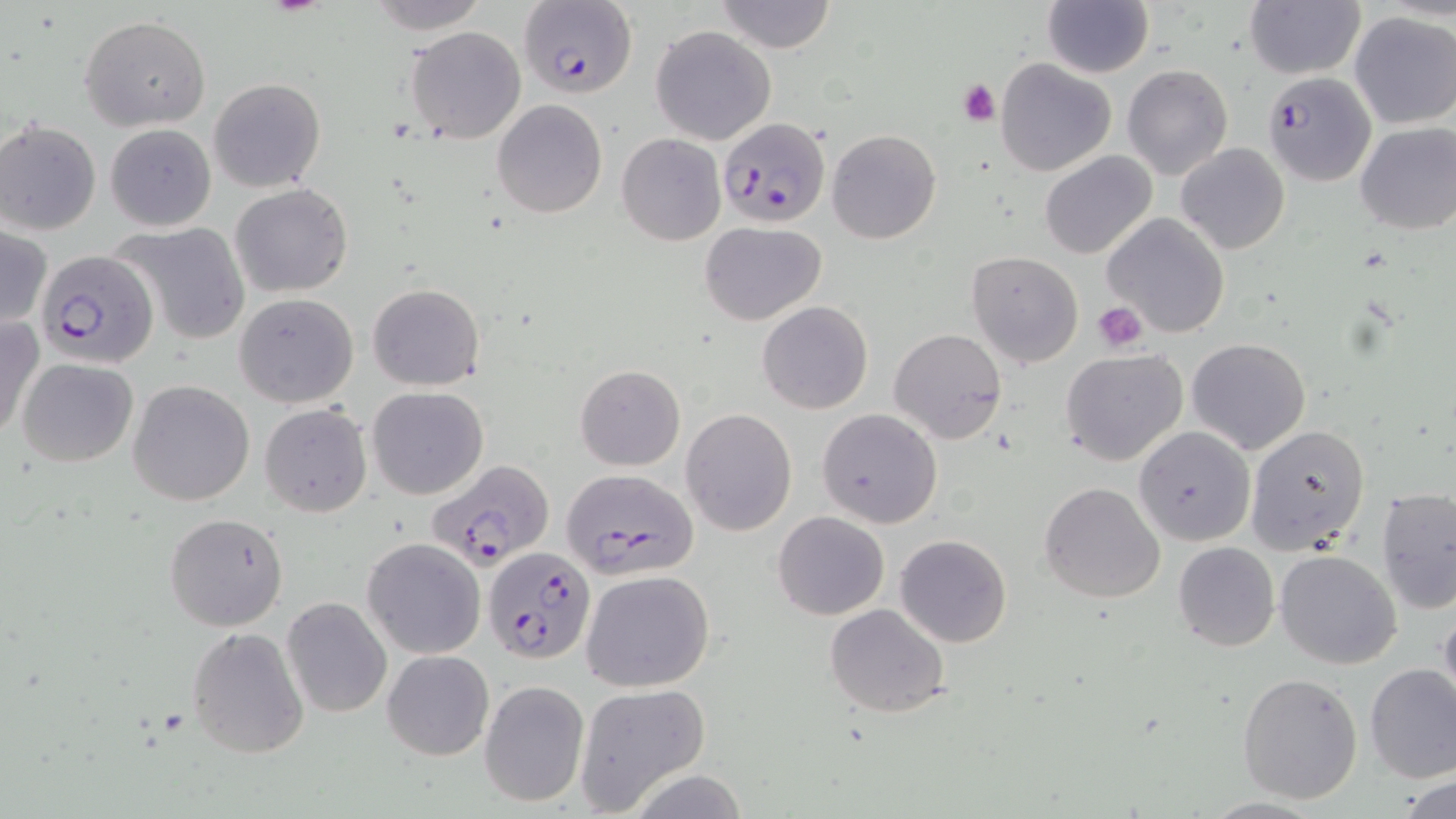

slide-level diagnosis = Plasmodium falciparum
magnification = 1000x
preparation = thin blood smear
platelet locations = approximate bounding boxes as (x1, y1, x2, y2) in pixels: (957, 78, 1001, 126), (1093, 301, 1150, 351)
Plasmodium falciparum-infected red blood cell locations = approximate bounding boxes as (x1, y1, x2, y2) in pixels: (519, 0, 636, 101), (1260, 71, 1377, 186), (717, 116, 832, 228), (36, 250, 158, 368), (425, 459, 556, 571), (559, 468, 700, 579), (484, 546, 594, 663)
field of view = single
stain = May-Grünwald-Giemsa
modality = optical microscopy
image size = 1456×819 pixels
uninfected red blood cell locations = approximate bounding boxes as (x1, y1, x2, y2) in pixels: (367, 0, 490, 33), (715, 0, 837, 53), (1244, 1, 1366, 79), (1043, 2, 1153, 77), (1348, 11, 1456, 129), (80, 16, 210, 131), (651, 25, 776, 145), (405, 27, 528, 145), (995, 57, 1116, 177), (1122, 64, 1231, 180), (207, 77, 326, 192), (493, 100, 607, 218), (1, 119, 101, 235), (1354, 121, 1455, 234), (105, 123, 216, 231), (827, 129, 941, 243), (616, 133, 725, 245), (1176, 143, 1290, 254), (1040, 150, 1157, 261), (230, 182, 353, 298), (1102, 213, 1230, 338), (699, 221, 828, 326), (110, 222, 251, 347), (0, 223, 49, 332), (966, 250, 1084, 368), (367, 283, 484, 389), (233, 292, 359, 409), (756, 301, 873, 415), (1, 316, 42, 443), (889, 328, 1006, 445), (1186, 337, 1311, 454), (1060, 349, 1188, 466), (17, 357, 138, 467), (576, 364, 685, 470), (128, 380, 256, 505), (367, 387, 489, 498), (260, 404, 373, 517), (682, 408, 797, 536), (817, 409, 942, 529), (1245, 424, 1371, 555), (1134, 427, 1255, 546), (1039, 482, 1164, 603), (1376, 487, 1456, 615), (772, 511, 889, 619), (164, 512, 289, 630), (895, 534, 1013, 647), (362, 537, 487, 659), (1173, 542, 1280, 651), (1275, 549, 1402, 668), (582, 570, 715, 693), (282, 596, 392, 718), (1437, 599, 1456, 718), (823, 603, 950, 717), (186, 626, 309, 757), (381, 649, 494, 760), (1365, 665, 1456, 782), (1236, 672, 1364, 805), (478, 680, 589, 808), (573, 684, 711, 814), (1398, 774, 1455, 818)